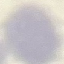
Malaria status: uninfected. Acquired by smartphone through the microscope eyepiece. Thin smear of blood. Giemsa-stained preparation. Automatically extracted cell patch, resized to 64 × 64 pixels.